Locate every Plasmodium parasite.
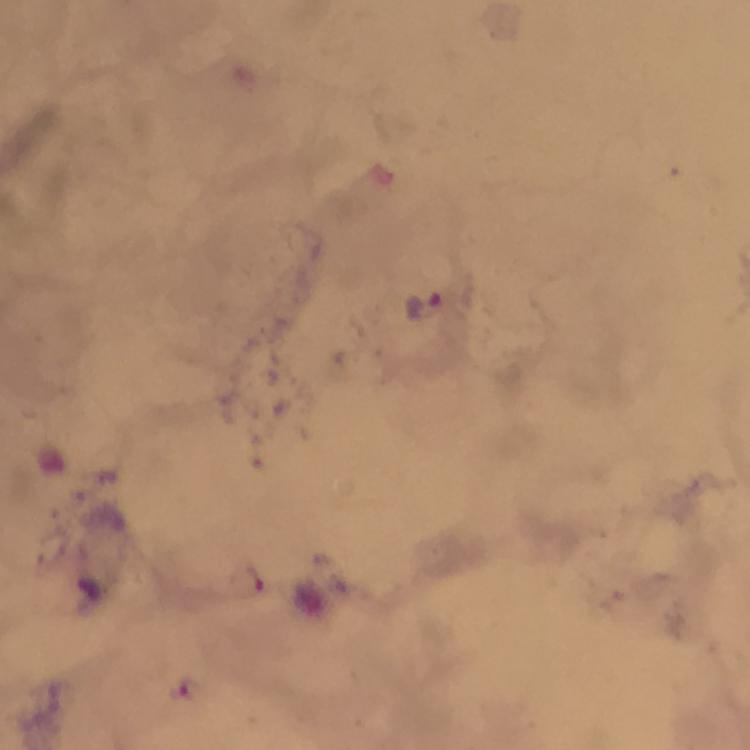

Approximate centers as (x, y) in pixels.
Plasmodium parasites: (424, 302), (256, 578), (187, 689).

Summary:
  - Context: from a diagnostic examination for malaria
  - Image size: 750×750 pixels
  - Magnification: 100x
  - Cropped from: a single field of view
  - Immersion oil: applied
  - Stain: Giemsa
  - Preparation: thick blood film
  - Capture: smartphone mounted on the microscope